State the preparation type.
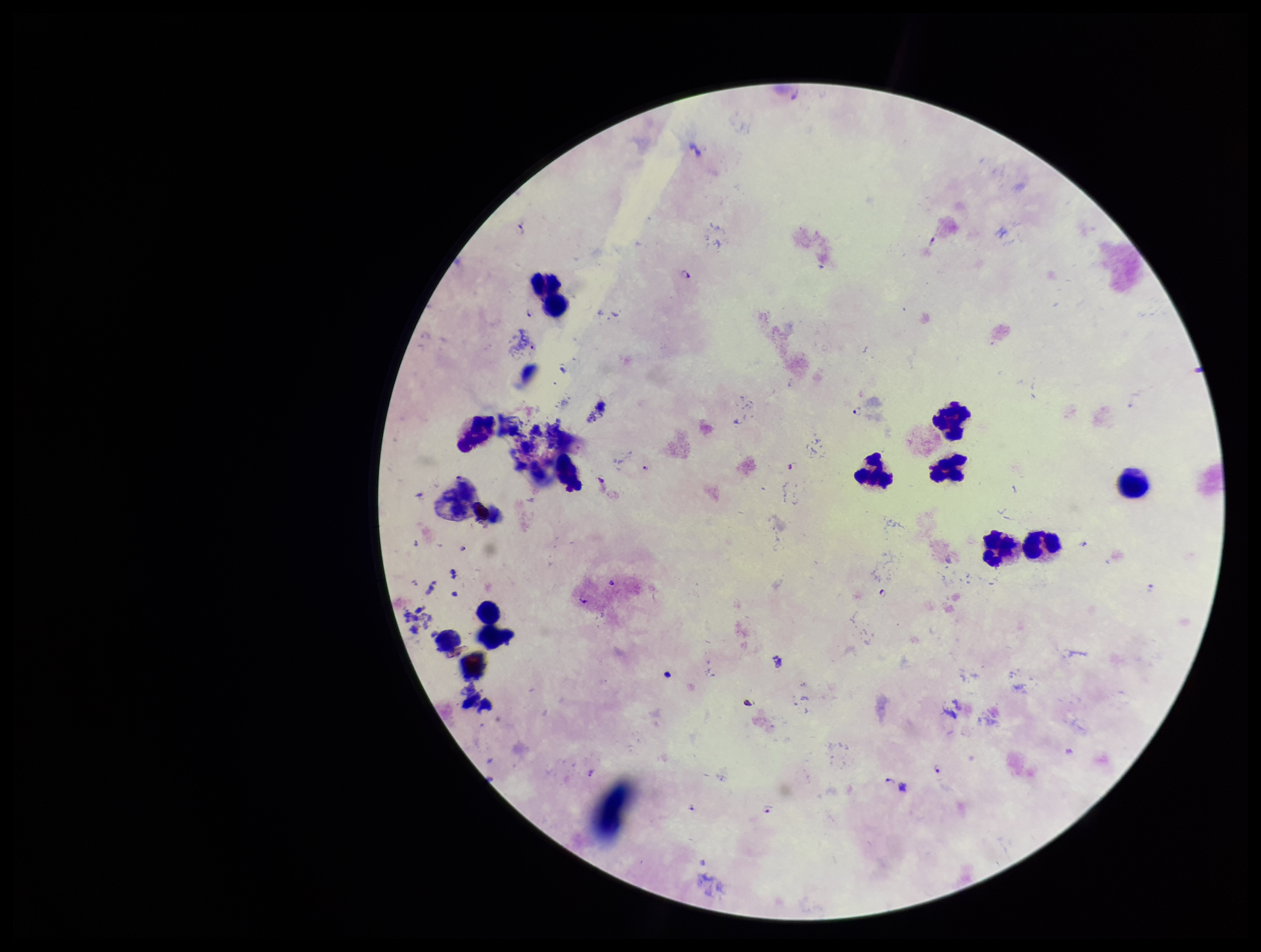
A thick smear.

Leukocyte count: 14. One field from this slide. Species reported for this patient: Plasmodium falciparum. Image is 1261×952 pixels. Patient malaria status: infected. Parasite count: 9. Plasmodium parasites: identified. Photographed through the microscope eyepiece with a smartphone camera. Stained with Giemsa.